Describe the morphology of the erythrocytes.
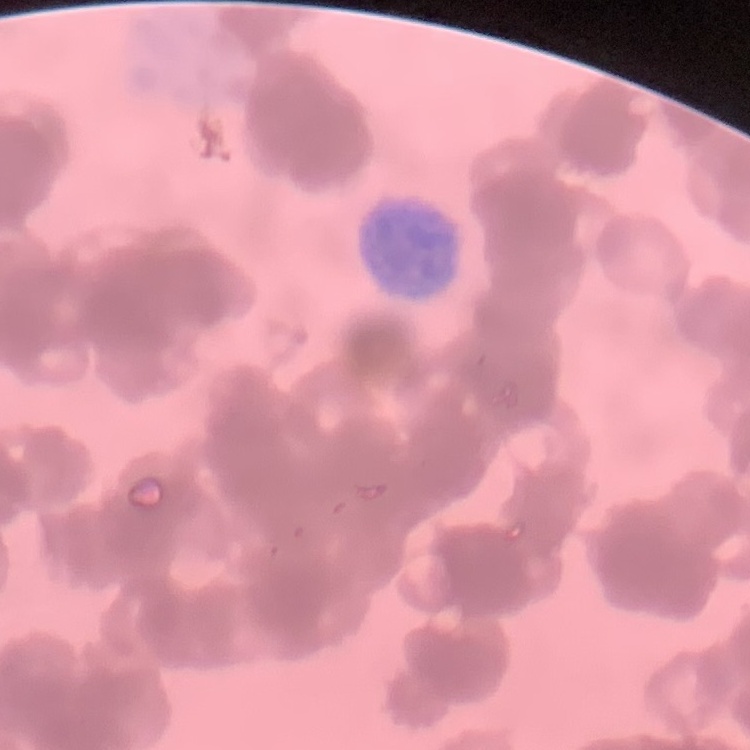
Rouleaux formation.

preparation = thin peripheral smear
stain = Field's or Giemsa
image type = one tile cut from a larger photomicrograph